State the blood parasite species.
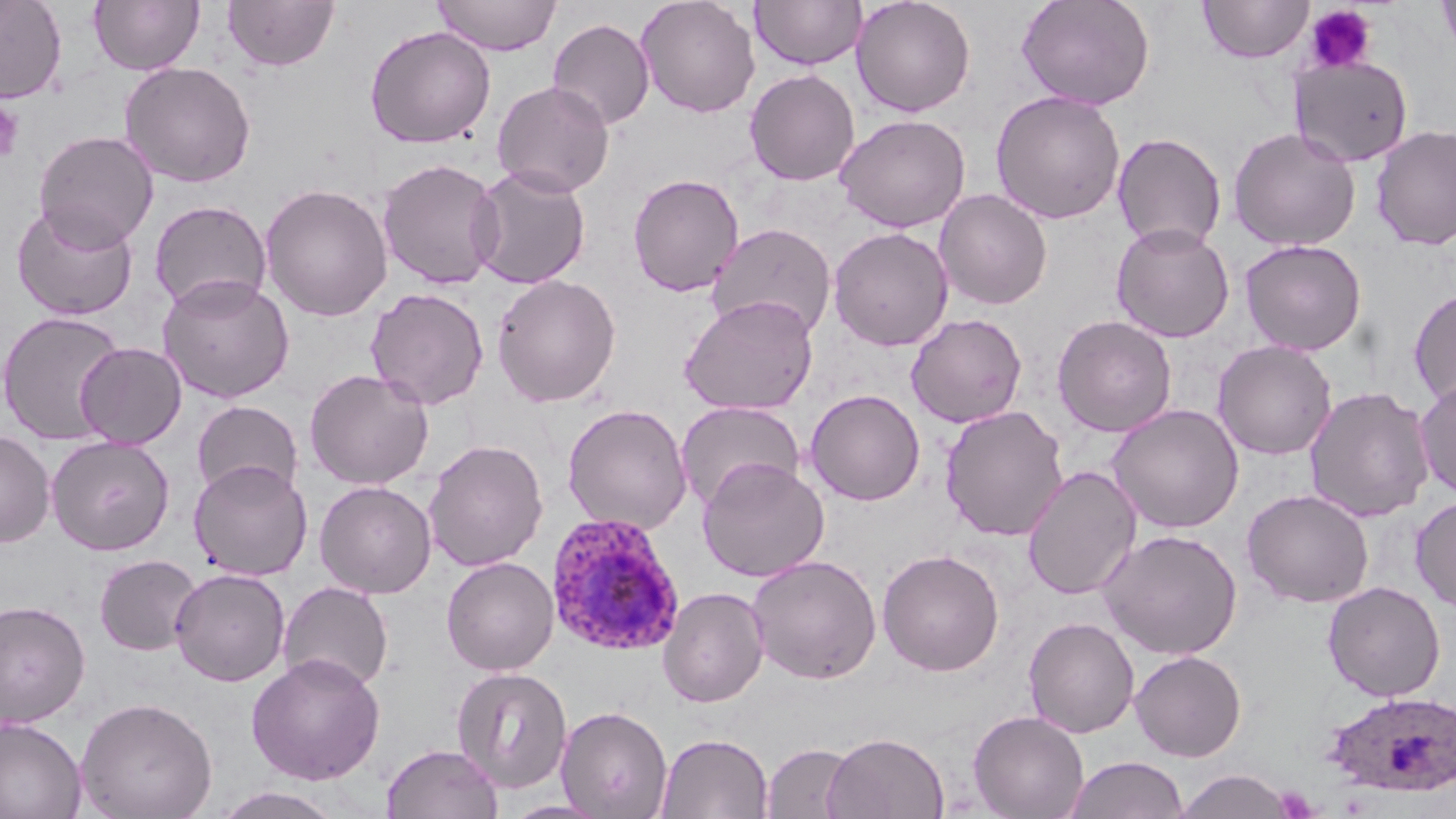

Plasmodium ovale.

Summary:
  - Coordinate format: approximate bounding boxes as (x1,y1)-(x2,y2) corner pairs in pixels
  - Plasmodium ovale-infected red blood cell locations: (545,512)-(686,657), (1323,691)-(1456,797)
  - Platelet locations: (1303,4)-(1377,74), (0,99)-(25,164)
  - Uninfected red blood cell locations: (0,0)-(67,103), (89,0)-(204,75), (222,0)-(339,71), (432,0)-(561,55), (635,0)-(760,118), (750,0)-(867,70), (851,0)-(976,117), (1017,0)-(1155,110), (1199,0)-(1313,64), (1437,0)-(1456,60), (548,18)-(655,130), (364,25)-(497,148), (1292,56)-(1413,167), (120,61)-(256,188), (744,69)-(861,186), (492,80)-(615,198), (990,90)-(1126,224), (835,114)-(971,232), (1371,124)-(1456,251), (1228,127)-(1361,251), (33,130)-(158,250), (1112,132)-(1227,252), (377,158)-(504,290), (468,164)-(591,290), (627,173)-(744,297), (259,183)-(394,322), (934,189)-(1052,310), (149,200)-(272,312), (12,202)-(139,321), (706,223)-(837,341), (1111,223)-(1235,342), (828,227)-(953,351), (1240,239)-(1367,356), (491,273)-(621,407), (157,275)-(295,403), (365,287)-(489,410), (1409,287)-(1456,409), (679,294)-(819,415), (0,310)-(127,446), (906,313)-(1027,428), (1051,315)-(1177,438), (1212,340)-(1337,460), (75,342)-(187,448), (304,368)-(434,490), (1415,377)-(1456,500), (1304,385)-(1435,523), (805,389)-(925,506), (192,400)-(303,502), (675,401)-(805,511), (562,403)-(693,535), (1107,403)-(1245,533), (939,405)-(1069,541), (0,429)-(55,547), (46,435)-(175,555), (423,439)-(549,571), (696,457)-(830,582), (188,459)-(312,581), (1022,465)-(1142,600), (314,480)-(437,599), (1242,489)-(1375,608), (1410,496)-(1456,612), (1098,529)-(1243,660), (877,549)-(1005,676), (93,554)-(202,656), (746,554)-(882,685), (441,556)-(558,675), (170,568)-(291,687), (278,581)-(394,693), (1322,581)-(1446,701), (657,587)-(769,708), (0,600)-(91,728), (1023,616)-(1140,738), (1129,650)-(1247,761), (246,652)-(386,785), (451,666)-(573,794), (75,697)-(217,819), (556,705)-(673,818), (968,710)-(1089,819), (0,717)-(86,819), (823,731)-(949,819), (656,732)-(773,818), (762,742)-(858,819), (381,743)-(504,819), (1064,755)-(1188,818), (1174,769)-(1295,818), (210,786)-(347,819), (501,799)-(614,818)
  - Field of view: one of a larger specimen
  - Stain: May-Grünwald-Giemsa
  - Image size: 1456×819 pixels
  - Modality: light microscopy
  - Preparation: thin blood smear
  - Magnification: 1000x